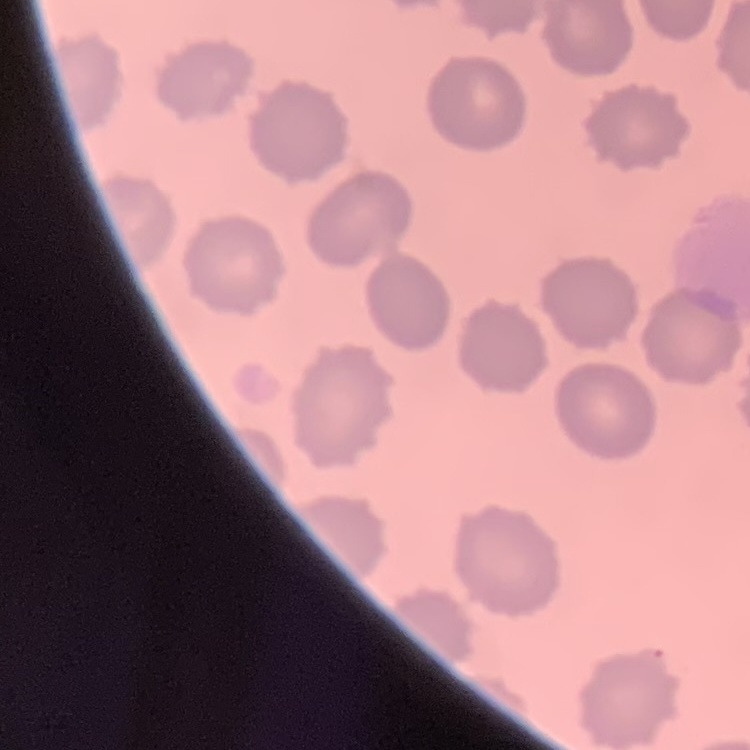
Summary:
  - Erythrocyte morphology: no rouleaux formation
  - Stain: Field's or Giemsa
  - Preparation: thin blood film
  - Image type: square crop of a larger photomicrograph